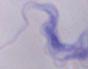
modality = photomicrograph
identification = trypanosome
magnification = 1000x